Assess this cell for malaria.
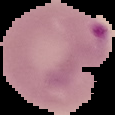
Parasitized.

Summary:
  - Image type: cell region segmented out of the field of view; surrounding area masked to black
  - Preparation: thin blood film
  - Image size: 115×115 pixels